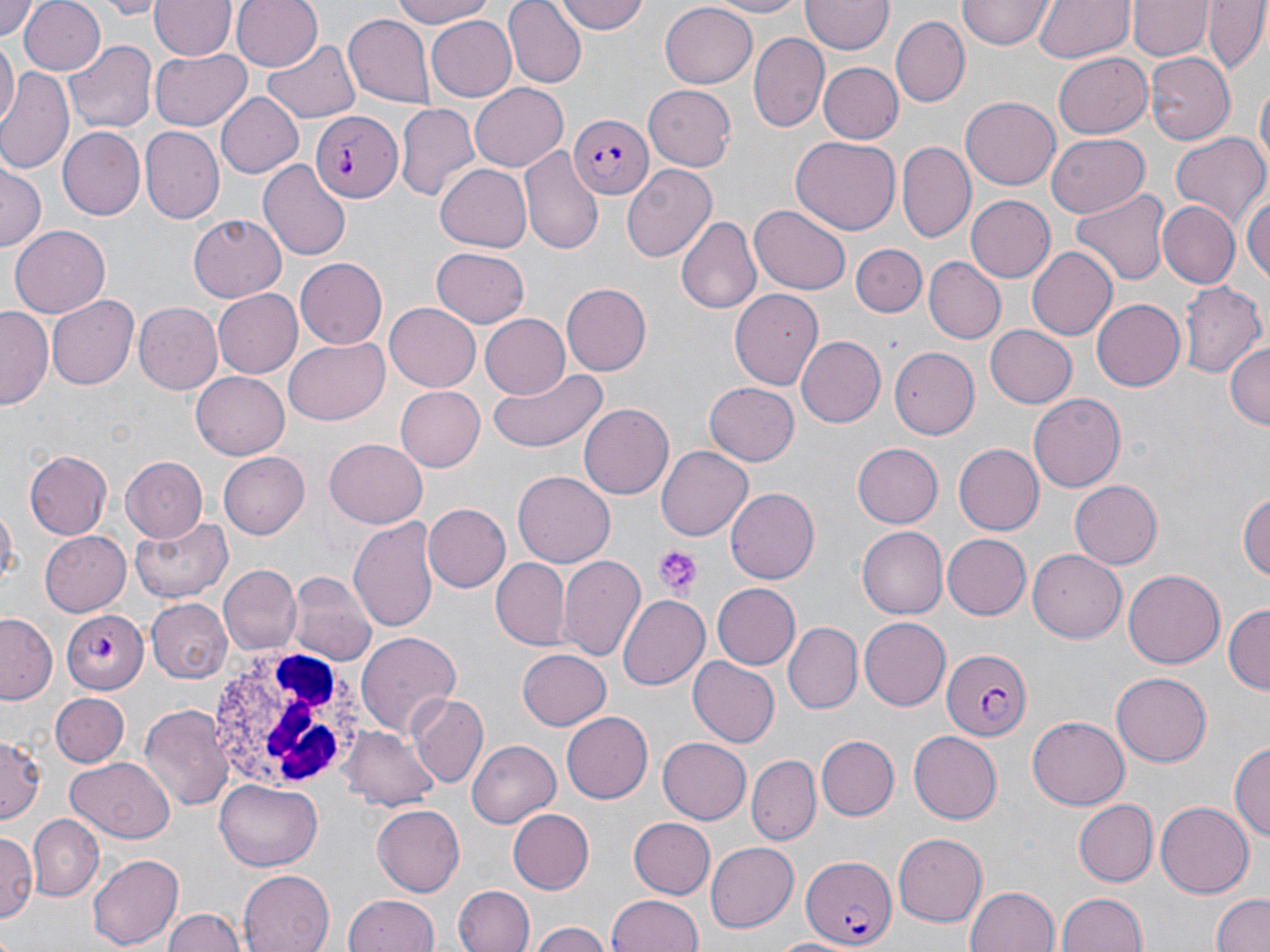

Approximate bounding boxes as named x1/y1/x2/y2 corners in pixels. White blood cell locations: (x1=206, y1=648, x2=365, y2=791). Platelet locations: (x1=654, y1=544, x2=699, y2=594). Plasmodium falciparum-infected red blood cell locations: (x1=310, y1=110, x2=401, y2=203), (x1=566, y1=113, x2=656, y2=200), (x1=58, y1=609, x2=148, y2=692), (x1=941, y1=648, x2=1033, y2=742), (x1=801, y1=854, x2=896, y2=948). Uninfected red blood cell locations: (x1=0, y1=0, x2=42, y2=39), (x1=17, y1=0, x2=105, y2=76), (x1=99, y1=0, x2=165, y2=18), (x1=233, y1=0, x2=322, y2=72), (x1=384, y1=0, x2=499, y2=28), (x1=503, y1=0, x2=587, y2=88), (x1=551, y1=0, x2=649, y2=36), (x1=699, y1=0, x2=811, y2=17), (x1=959, y1=0, x2=1054, y2=49), (x1=1034, y1=0, x2=1132, y2=64), (x1=150, y1=1, x2=235, y2=60), (x1=802, y1=1, x2=892, y2=56), (x1=1129, y1=1, x2=1209, y2=60), (x1=1203, y1=1, x2=1267, y2=75), (x1=661, y1=2, x2=756, y2=86), (x1=343, y1=12, x2=434, y2=106), (x1=425, y1=15, x2=517, y2=101), (x1=890, y1=16, x2=969, y2=108), (x1=749, y1=32, x2=828, y2=133), (x1=1, y1=36, x2=18, y2=128), (x1=262, y1=36, x2=360, y2=120), (x1=66, y1=37, x2=157, y2=132), (x1=150, y1=48, x2=251, y2=132), (x1=1055, y1=50, x2=1153, y2=135), (x1=1147, y1=54, x2=1236, y2=143), (x1=821, y1=62, x2=903, y2=144), (x1=0, y1=67, x2=76, y2=178), (x1=1254, y1=79, x2=1269, y2=182), (x1=470, y1=83, x2=567, y2=170), (x1=644, y1=83, x2=737, y2=171), (x1=215, y1=93, x2=305, y2=178), (x1=961, y1=94, x2=1060, y2=187), (x1=395, y1=104, x2=478, y2=204), (x1=57, y1=124, x2=145, y2=218), (x1=139, y1=126, x2=223, y2=222), (x1=1046, y1=133, x2=1151, y2=217), (x1=1168, y1=133, x2=1270, y2=234), (x1=790, y1=136, x2=901, y2=234), (x1=898, y1=142, x2=974, y2=243), (x1=521, y1=147, x2=605, y2=257), (x1=257, y1=159, x2=352, y2=263), (x1=0, y1=162, x2=46, y2=249), (x1=435, y1=162, x2=531, y2=250), (x1=622, y1=163, x2=718, y2=259), (x1=1071, y1=189, x2=1170, y2=286), (x1=1243, y1=190, x2=1269, y2=284), (x1=964, y1=193, x2=1055, y2=280), (x1=1157, y1=201, x2=1239, y2=290), (x1=750, y1=205, x2=848, y2=294), (x1=189, y1=212, x2=289, y2=301), (x1=678, y1=216, x2=761, y2=316), (x1=9, y1=226, x2=109, y2=319), (x1=850, y1=243, x2=925, y2=315), (x1=1025, y1=247, x2=1118, y2=340), (x1=431, y1=248, x2=531, y2=328), (x1=294, y1=257, x2=387, y2=348), (x1=923, y1=257, x2=1004, y2=344), (x1=1181, y1=280, x2=1265, y2=379), (x1=562, y1=284, x2=652, y2=376), (x1=212, y1=289, x2=302, y2=378), (x1=730, y1=289, x2=823, y2=390), (x1=47, y1=294, x2=138, y2=391), (x1=1090, y1=299, x2=1183, y2=392), (x1=134, y1=302, x2=223, y2=394), (x1=384, y1=303, x2=482, y2=392), (x1=1, y1=306, x2=52, y2=410), (x1=481, y1=312, x2=574, y2=399), (x1=985, y1=325, x2=1076, y2=407), (x1=797, y1=336, x2=885, y2=426), (x1=284, y1=338, x2=391, y2=424), (x1=1226, y1=343, x2=1269, y2=431), (x1=889, y1=348, x2=979, y2=436), (x1=488, y1=367, x2=607, y2=454), (x1=191, y1=373, x2=290, y2=459), (x1=704, y1=382, x2=799, y2=466), (x1=393, y1=385, x2=484, y2=472), (x1=1027, y1=393, x2=1125, y2=493), (x1=579, y1=404, x2=674, y2=501), (x1=325, y1=438, x2=427, y2=528), (x1=851, y1=443, x2=943, y2=528), (x1=656, y1=444, x2=753, y2=537), (x1=953, y1=445, x2=1043, y2=536), (x1=24, y1=450, x2=113, y2=539), (x1=218, y1=451, x2=309, y2=538), (x1=120, y1=457, x2=208, y2=543), (x1=514, y1=471, x2=614, y2=567), (x1=1070, y1=480, x2=1162, y2=569), (x1=1240, y1=487, x2=1270, y2=585), (x1=724, y1=488, x2=818, y2=585), (x1=1, y1=503, x2=19, y2=591), (x1=423, y1=503, x2=511, y2=593), (x1=348, y1=516, x2=439, y2=636), (x1=129, y1=517, x2=234, y2=601), (x1=857, y1=527, x2=948, y2=618), (x1=40, y1=532, x2=131, y2=616), (x1=942, y1=534, x2=1032, y2=619), (x1=1026, y1=550, x2=1126, y2=643), (x1=557, y1=553, x2=648, y2=663), (x1=490, y1=558, x2=570, y2=649), (x1=219, y1=564, x2=301, y2=654), (x1=1122, y1=570, x2=1226, y2=669), (x1=285, y1=572, x2=374, y2=663), (x1=710, y1=582, x2=801, y2=670), (x1=616, y1=593, x2=710, y2=690), (x1=148, y1=598, x2=231, y2=681), (x1=1223, y1=604, x2=1270, y2=694), (x1=0, y1=613, x2=60, y2=705), (x1=859, y1=617, x2=951, y2=710), (x1=782, y1=623, x2=861, y2=712), (x1=355, y1=632, x2=462, y2=739), (x1=517, y1=648, x2=612, y2=728), (x1=688, y1=658, x2=781, y2=747), (x1=1111, y1=671, x2=1212, y2=766), (x1=50, y1=693, x2=129, y2=767), (x1=409, y1=695, x2=489, y2=788), (x1=137, y1=704, x2=234, y2=811), (x1=561, y1=711, x2=653, y2=804), (x1=1027, y1=714, x2=1130, y2=808), (x1=343, y1=725, x2=439, y2=812), (x1=908, y1=731, x2=1003, y2=823), (x1=0, y1=733, x2=45, y2=821), (x1=818, y1=735, x2=898, y2=820), (x1=658, y1=738, x2=750, y2=823), (x1=1231, y1=739, x2=1269, y2=847), (x1=466, y1=740, x2=561, y2=829), (x1=747, y1=755, x2=822, y2=842), (x1=68, y1=757, x2=175, y2=841), (x1=215, y1=780, x2=323, y2=871), (x1=1074, y1=799, x2=1156, y2=885), (x1=1155, y1=801, x2=1255, y2=897), (x1=372, y1=805, x2=465, y2=894), (x1=508, y1=807, x2=594, y2=894), (x1=30, y1=815, x2=105, y2=899), (x1=628, y1=817, x2=716, y2=898), (x1=0, y1=831, x2=39, y2=923), (x1=893, y1=832, x2=987, y2=925), (x1=706, y1=840, x2=799, y2=930), (x1=87, y1=853, x2=182, y2=950), (x1=237, y1=869, x2=335, y2=952), (x1=453, y1=886, x2=534, y2=952), (x1=964, y1=887, x2=1059, y2=952), (x1=1055, y1=892, x2=1150, y2=952), (x1=344, y1=894, x2=440, y2=952), (x1=605, y1=894, x2=704, y2=952), (x1=1211, y1=895, x2=1270, y2=952), (x1=162, y1=910, x2=246, y2=952), (x1=530, y1=922, x2=608, y2=952), (x1=771, y1=937, x2=855, y2=952). Slide-level diagnosis: Plasmodium falciparum. Thin blood smear. One field of a larger specimen. Image is 1270×952 pixels. May-Grünwald-Giemsa-stained preparation. 1000x magnification. Light microscopy.